Identify the parasite.
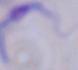
This is a trypanosome.

modality = micrograph
magnification = 1000x